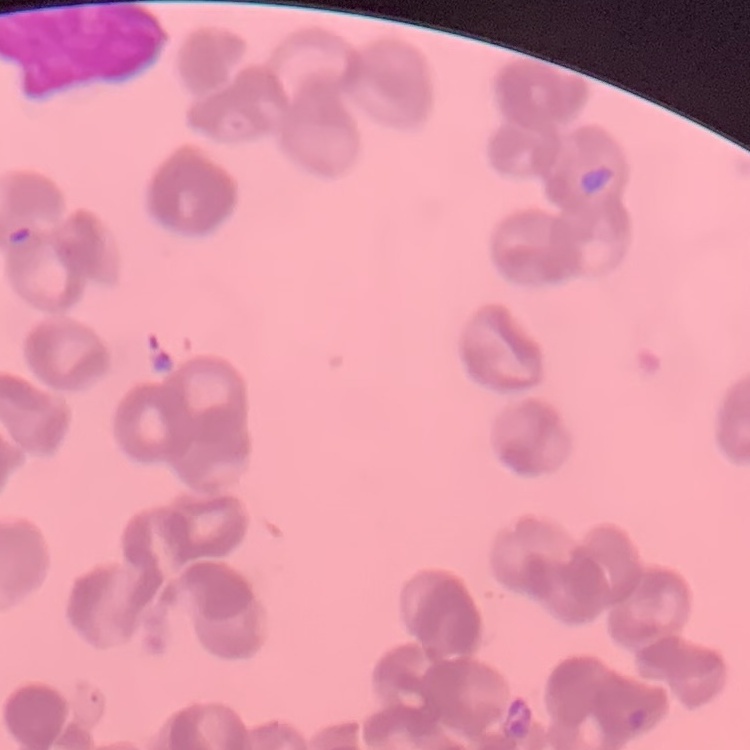
erythrocyte morphology = rouleaux formation
stain = Field's or Giemsa
preparation = thin blood smear
image type = one tile cut from a larger photomicrograph